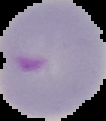

preparation = thin blood film
result = malaria parasites detected
image type = cell region segmented out of the field of view; surrounding area masked to black
image size = 106×121 pixels